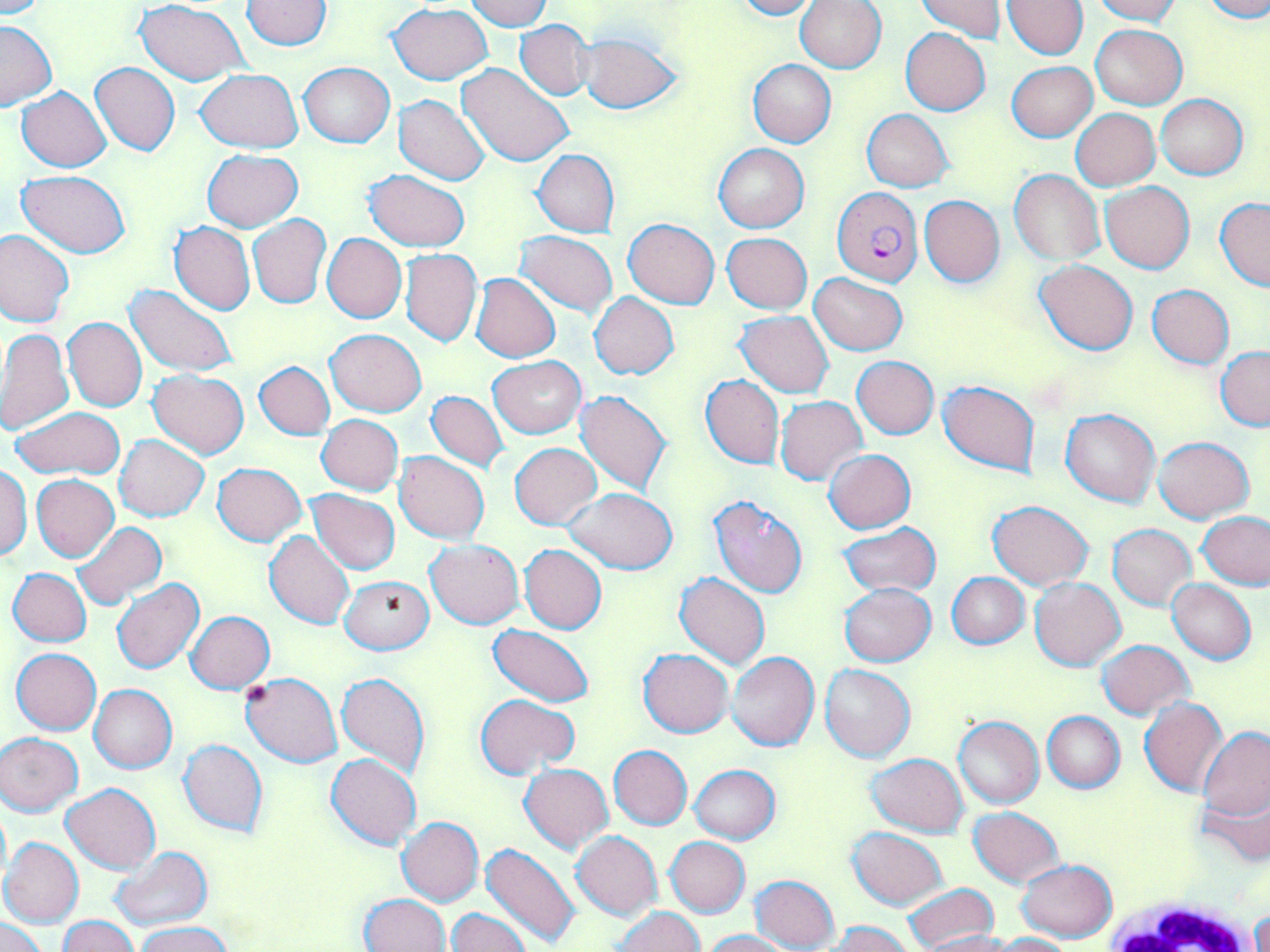 Approximate bounding boxes as (x1, y1, x2, y2) in pixels. White blood cell locations: (1089, 892, 1270, 952). Plasmodium falciparum-infected red blood cell locations: (831, 188, 923, 288). Uninfected red blood cell locations: (0, 0, 52, 19), (242, 0, 333, 50), (466, 0, 550, 29), (731, 0, 819, 19), (915, 0, 1011, 42), (1003, 0, 1087, 60), (1091, 0, 1181, 24), (1201, 0, 1270, 23), (137, 1, 250, 86), (794, 1, 887, 72), (387, 3, 494, 84), (514, 20, 592, 99), (0, 21, 56, 110), (1090, 23, 1188, 110), (900, 28, 991, 115), (579, 32, 682, 115), (747, 60, 835, 147), (1007, 61, 1097, 142), (90, 62, 180, 156), (299, 62, 394, 147), (457, 63, 574, 170), (196, 69, 304, 151), (17, 86, 112, 172), (394, 94, 491, 185), (1156, 94, 1248, 180), (1072, 108, 1159, 190), (862, 109, 953, 193), (713, 143, 809, 232), (202, 149, 302, 231), (533, 149, 619, 238), (364, 170, 470, 252), (1010, 170, 1103, 263), (18, 171, 129, 258), (1100, 180, 1194, 273), (918, 196, 1005, 286), (1216, 198, 1270, 292), (248, 213, 331, 309), (623, 218, 719, 308), (169, 221, 255, 315), (0, 229, 74, 328), (516, 231, 617, 316), (322, 233, 406, 324), (722, 233, 812, 314), (399, 249, 481, 347), (1034, 259, 1139, 355), (471, 273, 561, 362), (809, 274, 907, 355), (125, 284, 239, 376), (1148, 285, 1235, 368), (589, 293, 679, 379), (736, 311, 833, 398), (63, 318, 146, 412), (0, 329, 73, 437), (326, 329, 426, 417), (1216, 345, 1270, 431), (489, 356, 585, 438), (852, 356, 939, 439), (254, 361, 335, 439), (148, 371, 249, 458), (700, 375, 784, 469), (939, 380, 1039, 475), (576, 390, 673, 495), (425, 391, 510, 473), (775, 396, 867, 485), (11, 406, 125, 478), (1061, 408, 1160, 506), (316, 414, 404, 495), (1152, 435, 1255, 523), (115, 436, 208, 521), (511, 442, 601, 529), (824, 449, 916, 533), (394, 451, 489, 545), (212, 462, 306, 545), (0, 464, 32, 560), (232, 464, 328, 593), (31, 475, 119, 562), (564, 487, 678, 574), (308, 489, 400, 574), (707, 495, 809, 598), (988, 499, 1093, 589), (1198, 511, 1270, 590), (72, 521, 167, 609), (837, 523, 940, 596), (1108, 524, 1196, 610), (265, 530, 355, 629), (425, 540, 523, 628), (519, 544, 607, 634), (9, 568, 91, 647), (947, 572, 1029, 649), (674, 573, 771, 671), (340, 575, 434, 655), (1029, 576, 1127, 670), (112, 577, 205, 674), (1167, 580, 1256, 664), (838, 583, 937, 666), (186, 611, 274, 692), (489, 624, 594, 707), (1097, 639, 1193, 719), (11, 648, 101, 735), (638, 648, 734, 738), (727, 652, 820, 752), (820, 663, 914, 761), (240, 672, 343, 767), (337, 672, 431, 778), (88, 684, 176, 773), (476, 693, 579, 780), (1139, 698, 1228, 797), (1044, 711, 1125, 792), (953, 716, 1045, 808), (1199, 727, 1270, 822), (0, 732, 83, 815), (179, 739, 269, 837), (609, 745, 692, 830), (326, 753, 422, 849), (866, 753, 969, 836), (520, 763, 612, 851), (690, 765, 779, 844), (62, 783, 160, 874), (1199, 785, 1270, 867), (0, 801, 10, 887), (968, 807, 1065, 887), (397, 816, 484, 906), (848, 827, 948, 909), (571, 831, 662, 919), (1, 837, 83, 927), (665, 837, 750, 917), (481, 843, 583, 948), (109, 848, 209, 930), (1016, 859, 1115, 942), (751, 875, 840, 951), (901, 883, 999, 951), (360, 893, 451, 952), (615, 906, 703, 952), (446, 907, 530, 952), (1248, 908, 1269, 952), (57, 915, 139, 952), (1, 917, 50, 952), (827, 921, 910, 952), (136, 922, 235, 952), (702, 929, 788, 951), (922, 931, 1021, 952), (991, 932, 1075, 951). Slide-level diagnosis: Plasmodium falciparum. May-Grünwald-Giemsa-stained preparation. Single field of view. Optical microscopy. Captured at 1000x magnification. Image is 1270×952 pixels. Thin blood smear.